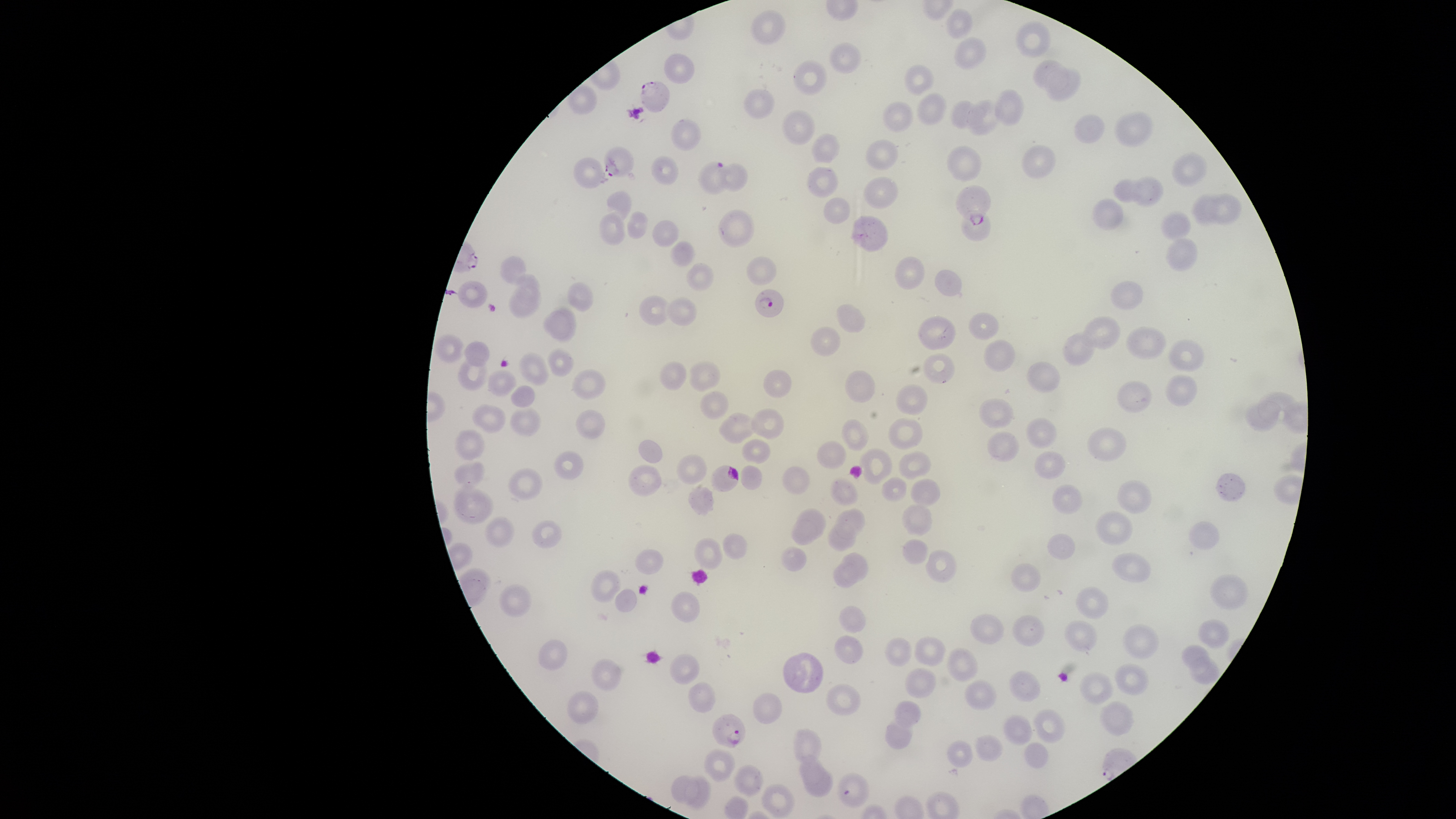
Approximate bounding boxes as {left, top, right, bottom} in pixels.
Summary:
  - Uninfected red blood cells: {945, 8, 973, 39}, {750, 10, 786, 46}, {1015, 20, 1051, 58}, {953, 36, 987, 68}, {828, 42, 861, 74}, {663, 53, 695, 84}, {1032, 59, 1069, 92}, {792, 60, 827, 96}, {904, 64, 936, 96}, {1045, 67, 1081, 101}, {743, 88, 775, 119}, {992, 88, 1024, 126}, {917, 93, 947, 125}, {965, 99, 998, 137}, {950, 100, 990, 130}, {882, 101, 914, 132}, {781, 110, 815, 145}, {1113, 112, 1154, 148}, {1074, 115, 1105, 144}, {670, 118, 701, 151}, {811, 133, 841, 163}, {865, 139, 898, 171}, {1020, 144, 1057, 178}, {946, 145, 981, 181}, {1170, 150, 1209, 187}, {650, 155, 679, 185}, {573, 157, 608, 189}, {715, 163, 749, 191}, {807, 166, 840, 198}, {863, 176, 898, 209}, {1130, 176, 1165, 206}, {1113, 178, 1147, 203}, {606, 190, 632, 227}, {1205, 192, 1241, 224}, {1190, 195, 1220, 227}, {1091, 197, 1125, 230}, {823, 198, 851, 223}, {717, 209, 755, 248}, {599, 210, 626, 246}, {1160, 210, 1192, 241}, {625, 211, 648, 239}, {959, 211, 991, 241}, {850, 214, 889, 252}, {652, 220, 680, 247}, {1166, 238, 1198, 272}, {669, 240, 695, 267}, {499, 255, 526, 284}, {746, 256, 777, 286}, {895, 256, 925, 290}, {685, 263, 714, 291}, {935, 269, 962, 297}, {515, 273, 540, 307}, {1109, 281, 1143, 310}, {566, 282, 594, 312}, {508, 284, 542, 319}, {639, 295, 674, 326}, {666, 296, 698, 325}, {837, 303, 866, 333}, {543, 306, 577, 342}, {968, 313, 999, 340}, {918, 315, 956, 350}, {1081, 315, 1121, 350}, {810, 326, 841, 357}, {1125, 326, 1168, 360}, {1062, 331, 1096, 366}, {433, 333, 464, 364}, {983, 339, 1016, 372}, {1168, 339, 1205, 372}, {463, 341, 490, 367}, {547, 348, 575, 378}, {518, 351, 550, 386}, {923, 353, 955, 384}, {456, 357, 489, 391}, {689, 360, 721, 392}, {658, 361, 686, 391}, {1026, 361, 1060, 394}, {571, 368, 606, 400}, {762, 369, 792, 397}, {487, 370, 517, 396}, {844, 370, 876, 403}, {1165, 375, 1198, 406}, {1116, 381, 1152, 413}, {895, 384, 928, 415}, {510, 385, 535, 407}, {700, 390, 729, 420}, {978, 396, 1014, 429}, {1243, 400, 1282, 432}, {471, 404, 507, 434}, {510, 406, 542, 437}, {751, 407, 785, 440}, {575, 409, 606, 438}, {718, 411, 761, 444}, {888, 417, 923, 449}, {1025, 417, 1057, 448}, {841, 419, 869, 451}, {1087, 426, 1127, 462}, {453, 427, 485, 461}, {987, 431, 1020, 462}, {740, 437, 771, 465}, {638, 439, 663, 463}, {817, 441, 847, 469}, {858, 448, 892, 485}, {1034, 450, 1066, 479}, {554, 451, 584, 480}, {898, 451, 931, 480}, {675, 453, 708, 484}, {454, 461, 485, 489}, {627, 464, 662, 497}, {740, 464, 763, 490}, {782, 465, 810, 495}, {507, 467, 544, 501}, {1216, 472, 1246, 502}, {829, 477, 858, 506}, {881, 477, 908, 501}, {910, 479, 941, 507}, {453, 480, 493, 524}, {1117, 480, 1152, 513}, {1052, 484, 1083, 515}, {688, 486, 715, 516}, {901, 503, 932, 536}, {796, 507, 827, 539}, {834, 507, 865, 539}, {1094, 510, 1132, 546}, {483, 516, 515, 548}, {791, 517, 818, 545}, {531, 520, 562, 548}, {1188, 521, 1220, 550}, {827, 522, 857, 551}, {722, 533, 748, 559}, {1046, 534, 1075, 560}, {693, 538, 722, 570}, {902, 539, 929, 565}, {780, 547, 807, 571}, {635, 549, 664, 575}, {925, 549, 957, 583}, {841, 552, 868, 582}, {1111, 552, 1151, 583}, {832, 563, 858, 589}, {1010, 563, 1041, 592}, {590, 570, 621, 602}, {1209, 574, 1249, 611}, {499, 584, 532, 617}, {1076, 586, 1108, 619}, {614, 588, 637, 612}, {671, 591, 700, 623}, {838, 604, 867, 633}, {969, 614, 1005, 644}, {1011, 614, 1045, 646}, {1064, 619, 1097, 652}, {1197, 619, 1230, 649}, {1122, 624, 1159, 659}, {834, 634, 864, 665}, {884, 636, 913, 667}, {914, 636, 947, 667}, {537, 639, 568, 670}, {1181, 644, 1211, 674}, {947, 646, 979, 682}, {782, 651, 823, 693}, {669, 653, 701, 685}, {1190, 656, 1219, 685}, {590, 658, 622, 691}, {1114, 662, 1149, 696}, {903, 666, 937, 698}, {1008, 669, 1042, 703}, {1079, 671, 1112, 705}, {963, 679, 997, 712}, {688, 681, 716, 713}, {824, 683, 861, 716}, {567, 688, 599, 723}, {752, 692, 783, 724}, {894, 699, 921, 729}, {1100, 701, 1133, 737}, {1032, 708, 1066, 744}, {1002, 714, 1034, 745}, {884, 719, 912, 750}, {792, 728, 822, 763}, {974, 734, 1002, 762}, {947, 739, 973, 768}, {1024, 742, 1048, 769}, {704, 748, 736, 782}, {799, 755, 826, 786}, {733, 765, 764, 797}, {805, 771, 833, 798}, {836, 772, 869, 808}, {671, 775, 699, 805}, {685, 775, 712, 809}, {760, 783, 795, 818}
  - Parasitized red blood cells: {639, 81, 670, 114}, {603, 145, 634, 177}, {696, 160, 732, 194}, {954, 185, 991, 225}, {754, 288, 784, 318}, {710, 465, 739, 492}, {712, 713, 745, 747}
  - Capture: smartphone photograph through the microscope eyepiece
  - Preparation: thin blood smear
  - Presence: malaria parasites seen
  - Stain: Giemsa
  - Image size: 1456×819 pixels
  - Field of view: single
  - Visible region: circular
  - Species: Plasmodium falciparum